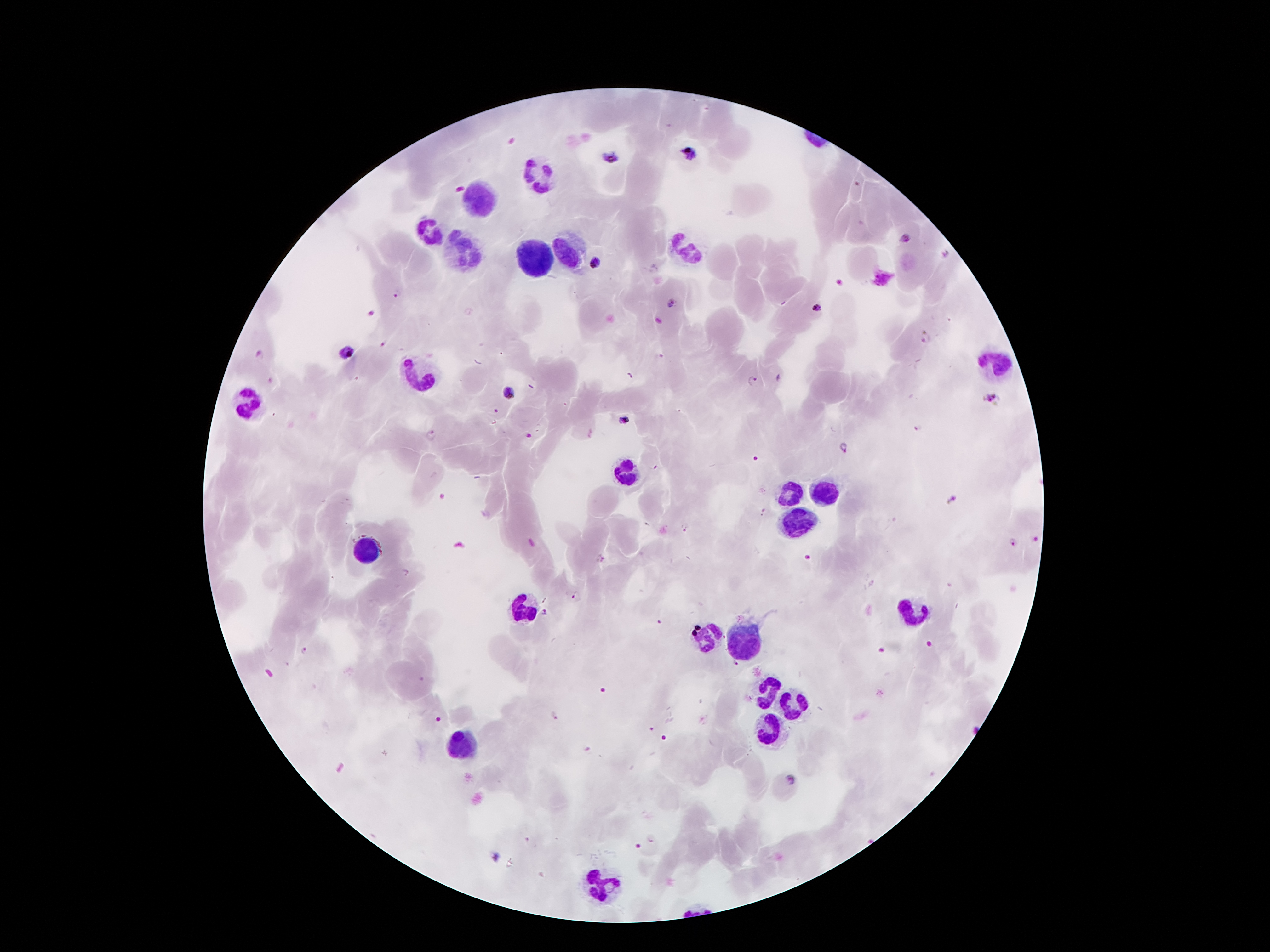

Approximate centers as [x, y] in pixels. Plasmodium parasite locations: [688, 153], [609, 156], [904, 239], [594, 262], [838, 282], [671, 302], [814, 308], [372, 313], [926, 337], [347, 352], [753, 381], [508, 394], [991, 399], [495, 410], [624, 420], [918, 427], [430, 435], [528, 436], [845, 447], [950, 501], [684, 527], [1033, 540], [1013, 542], [576, 596], [545, 614], [304, 650], [734, 665], [554, 714], [588, 749], [790, 779], [652, 839], [495, 857]. Leukocyte locations: [537, 174], [482, 200], [430, 233], [684, 249], [461, 250], [572, 258], [533, 260], [992, 363], [421, 376], [249, 401], [621, 475], [822, 493], [789, 498], [799, 519], [364, 552], [528, 609], [912, 611], [709, 638], [744, 639], [768, 689], [789, 702], [770, 729], [459, 745], [604, 878]. 100x magnification. Patient malaria status: positive for Plasmodium falciparum. Giemsa stain. Image is 1270×952 pixels. Thick peripheral-blood smear. Smartphone photograph taken through the microscope eyepiece. One field from this slide.